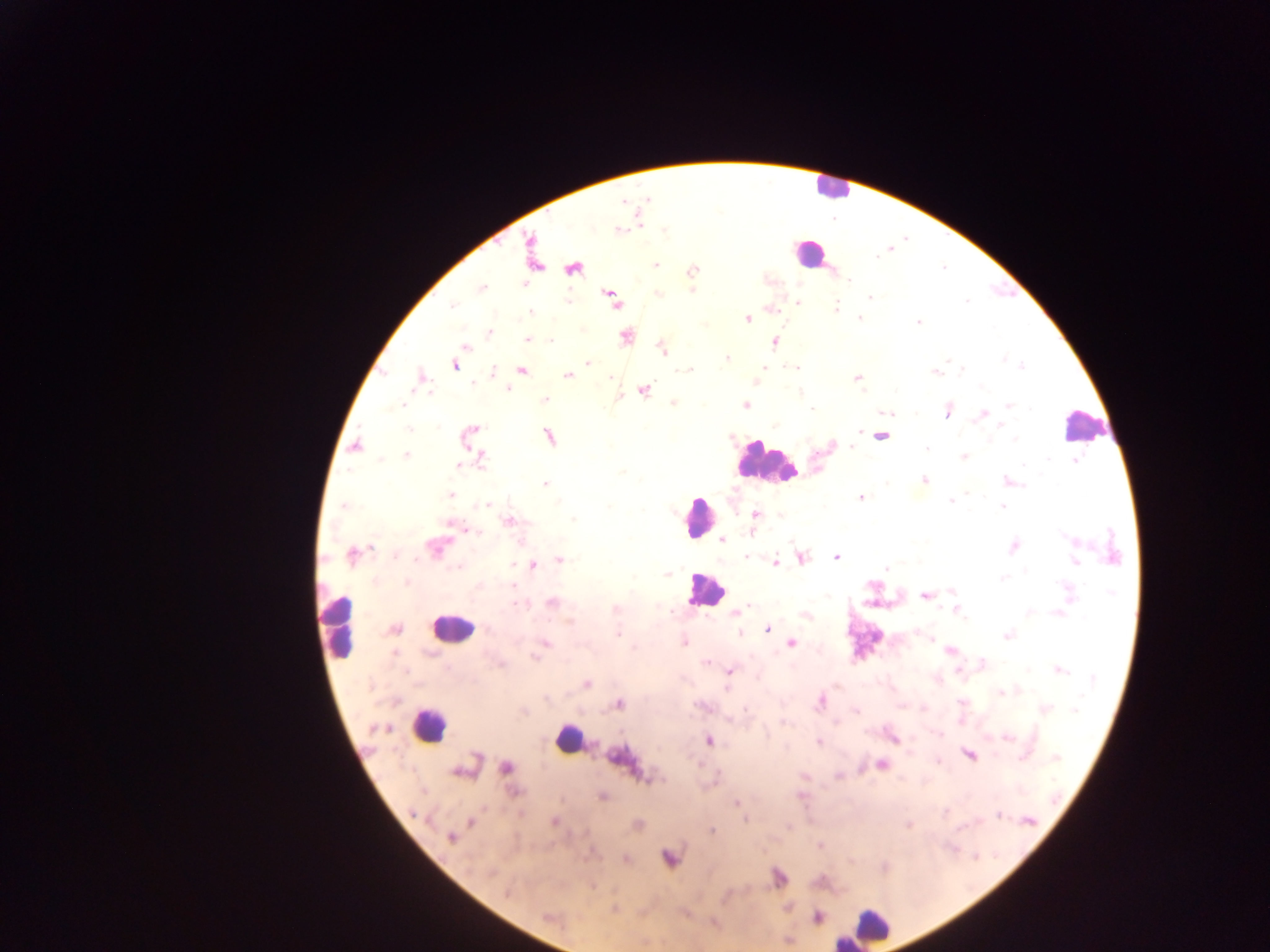
Approximate centers as {x, y} in pixels. Leukocyte locations: {831, 187}, {808, 254}, {1084, 426}, {763, 461}, {697, 517}, {705, 589}, {340, 628}, {451, 628}, {428, 725}, {566, 739}, {870, 927}. Plasmodium parasite locations: {623, 201}, {638, 218}, {619, 229}, {533, 256}, {654, 264}, {573, 267}, {691, 270}, {480, 287}, {693, 289}, {870, 297}, {612, 298}, {797, 302}, {747, 318}, {917, 321}, {489, 332}, {625, 337}, {528, 340}, {775, 341}, {464, 347}, {661, 348}, {726, 359}, {588, 363}, {455, 365}, {763, 368}, {521, 369}, {796, 369}, {935, 372}, {492, 373}, {566, 375}, {857, 377}, {421, 379}, {643, 389}, {544, 400}, {673, 402}, {746, 405}, {947, 411}, {891, 413}, {982, 414}, {469, 435}, {880, 435}, {549, 436}, {355, 446}, {853, 448}, {405, 454}, {964, 456}, {480, 459}, {1077, 462}, {458, 465}, {924, 479}, {1008, 482}, {545, 483}, {450, 495}, {861, 497}, {1002, 505}, {755, 513}, {509, 521}, {520, 540}, {722, 540}, {1013, 545}, {436, 547}, {352, 555}, {801, 557}, {836, 557}, {559, 559}, {1075, 561}, {774, 562}, {532, 565}, {885, 567}, {667, 573}, {406, 582}, {925, 595}, {552, 603}, {748, 606}, {955, 608}, {736, 613}, {805, 614}, {394, 628}, {766, 628}, {1007, 635}, {931, 636}, {684, 642}, {791, 643}, {544, 644}, {949, 651}, {705, 661}, {981, 664}, {1058, 669}, {729, 670}, {586, 683}, {1001, 692}, {819, 701}, {619, 704}, {1044, 709}, {1006, 736}, {892, 738}, {709, 740}, {819, 742}, {969, 755}, {620, 760}, {881, 764}, {505, 767}, {463, 769}, {602, 796}, {736, 803}, {554, 821}, {471, 822}, {637, 825}, {909, 825}, {788, 826}, {712, 830}, {450, 836}, {821, 846}, {668, 858}, {625, 859}, {778, 878}, {614, 908}, {817, 917}, {550, 918}, {788, 941}. Photographed through a microscope with a mobile-phone camera. Collected in Ghana. Image is 1270×952 pixels. One field of view. Thick blood smear.